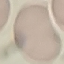

Summary:
  - Result: no malaria parasites detected
  - Image type: automatically extracted cell patch, resized to 64 × 64 pixels
  - Stain: Giemsa
  - Preparation: thin blood film
  - Capture: smartphone camera at the microscope eyepiece